Point out each Plasmodium parasite and each leukocyte.
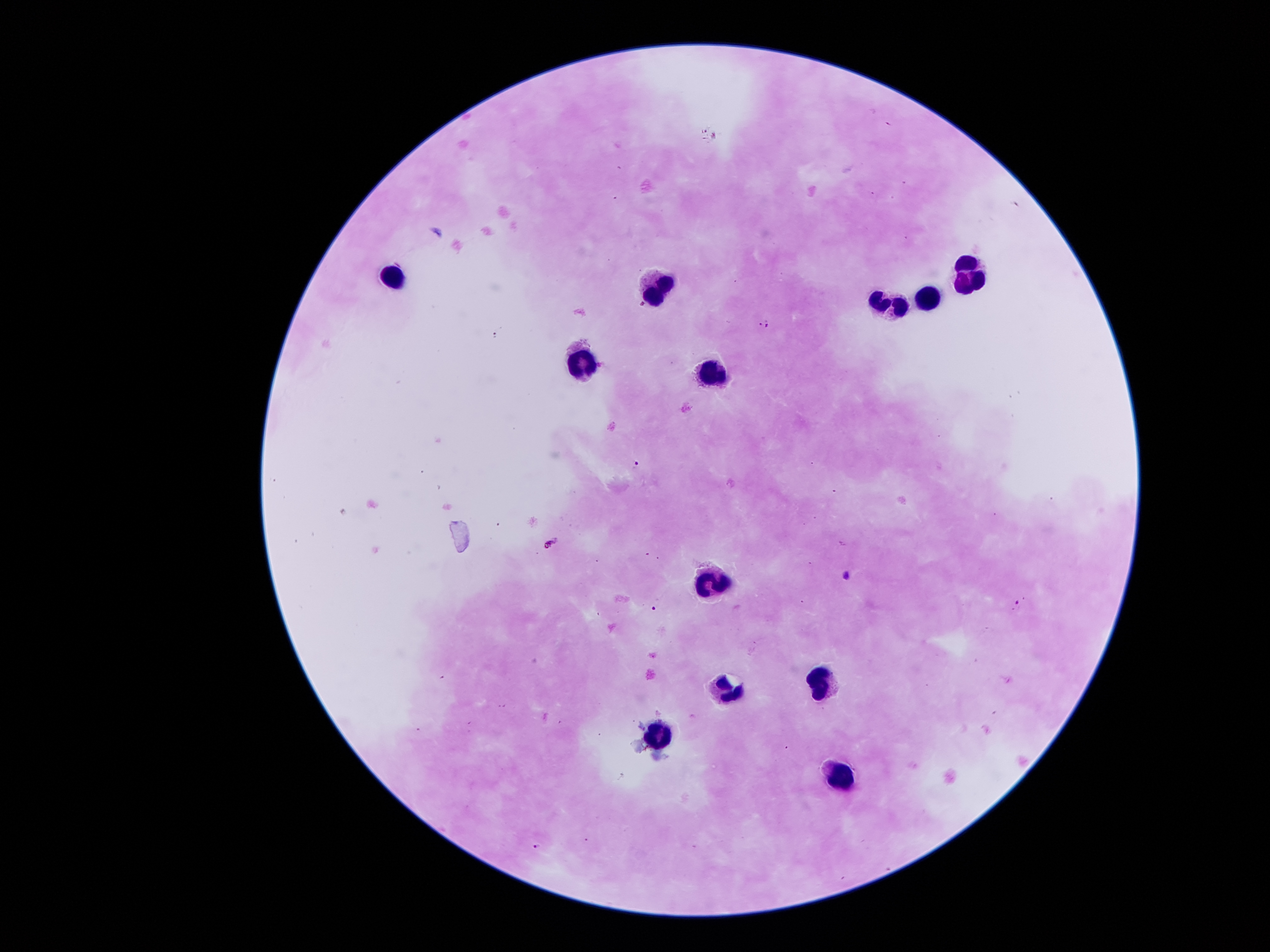

Approximate centers as [x, y] in pixels.
Plasmodium parasites: [766, 323], [637, 465], [550, 543], [847, 575], [1018, 603], [655, 609], [538, 847].
Leukocytes: [971, 272], [391, 282], [660, 282], [934, 297], [889, 309], [583, 367], [707, 370], [709, 578], [822, 681], [726, 689], [656, 733], [839, 779].

{
  "image_size": "1270×952 pixels",
  "stain": "Giemsa",
  "capture": "smartphone through the microscope eyepiece",
  "preparation": "thick blood smear",
  "patient_malaria_status": "infected with Plasmodium falciparum",
  "magnification": "100x",
  "field_of_view": "single"
}